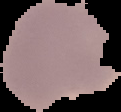

image_type: segmented cell region with the area outside set to black
malaria_status: parasitized
preparation: thin blood smear
image_size: 121×112 pixels